Comment on the morphology of the red blood cells.
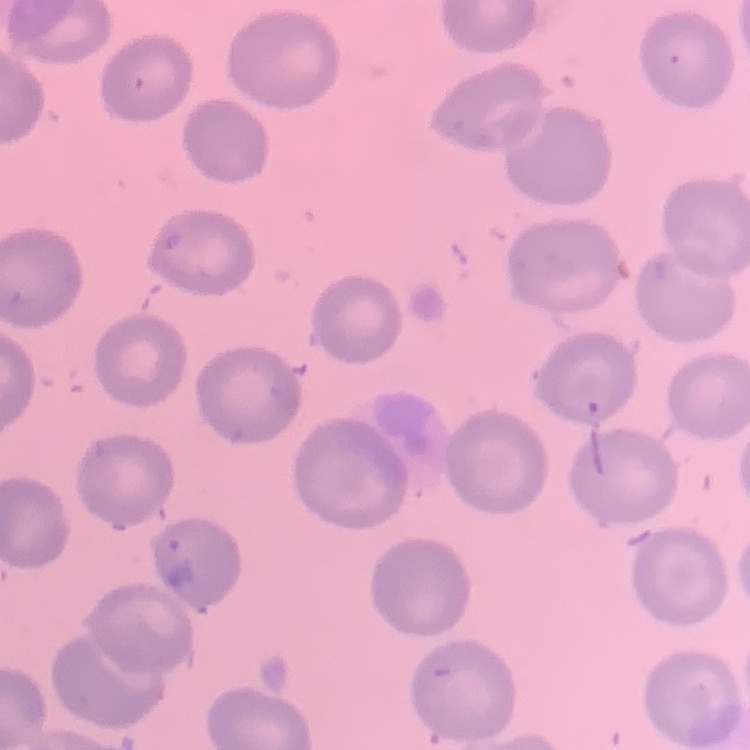

No rouleaux formation.

Summary:
  - Stain: Field's or Giemsa
  - Preparation: thin blood smear
  - Image type: one tile cut from a larger photomicrograph